Classify this cell by malaria status.
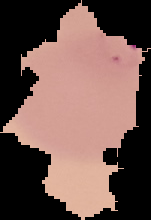
It is parasitized.

{
  "image_size": "151×220 pixels",
  "preparation": "thin blood film",
  "image_type": "cell region segmented out of the field of view; surrounding area masked to black"
}